Assess this cell for malaria.
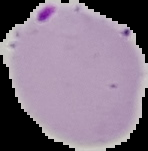
Parasitized.

From a thin blood smear. Image is 148×151 pixels. Segmented cell region on a black background.